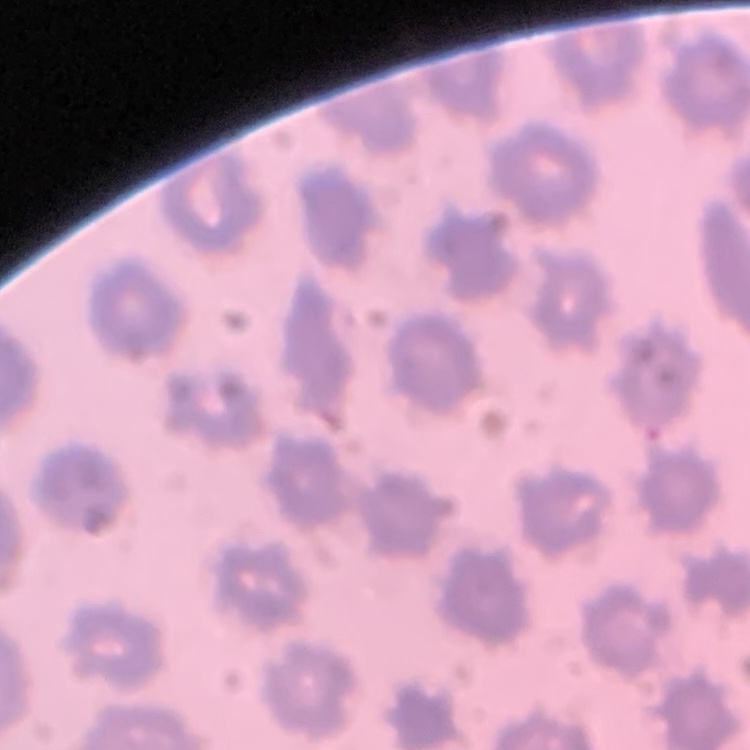
red blood cell morphology = no rouleaux formation
preparation = thin peripheral smear
stain = Field's or Giemsa
image type = square crop of a larger photomicrograph